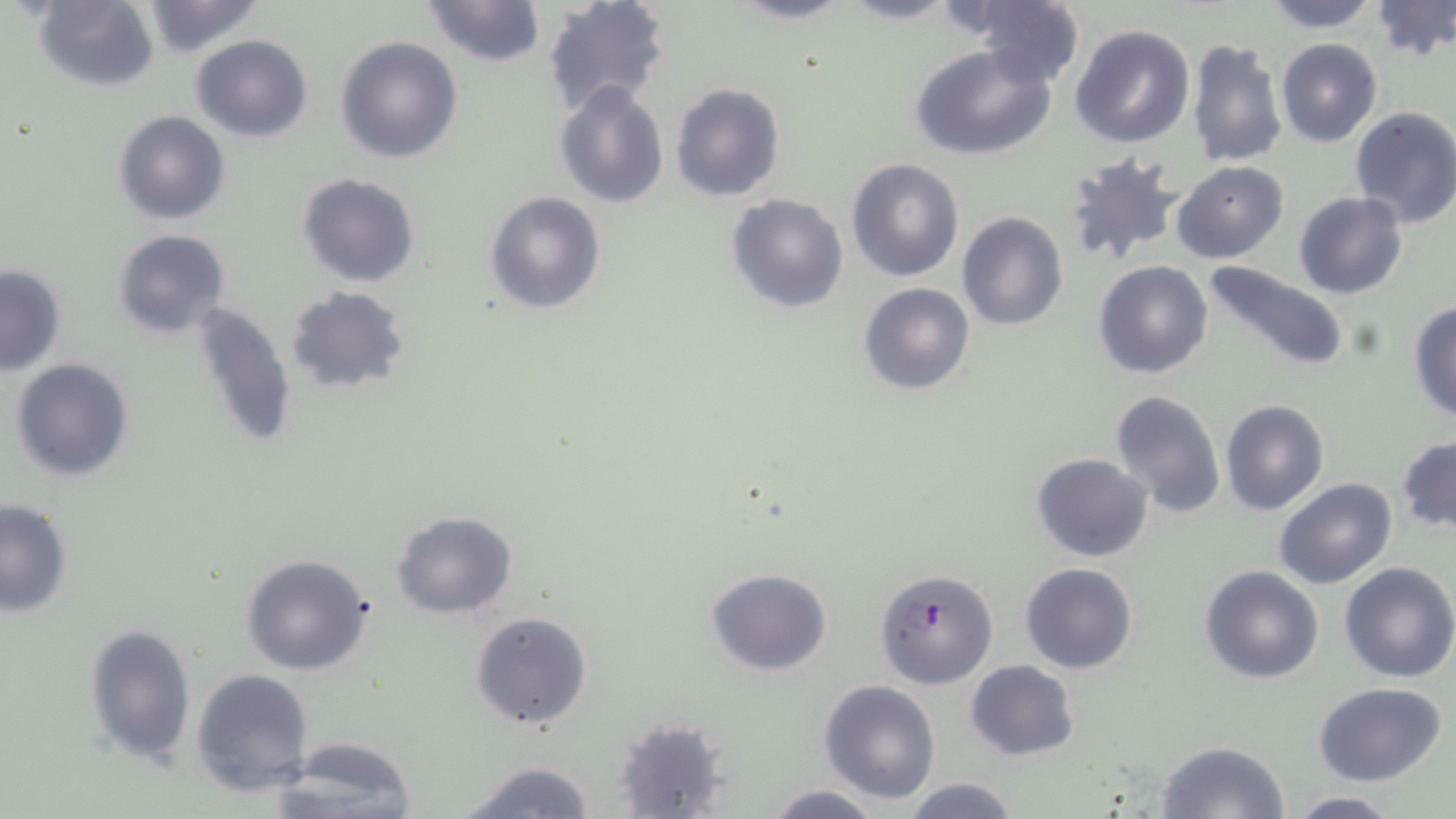

Approximate bounding boxes as named x1/y1/x2/y2 corners in pixels. Uninfected red blood cell locations: (x1=32, y1=0, x2=158, y2=91), (x1=137, y1=0, x2=268, y2=57), (x1=420, y1=0, x2=547, y2=69), (x1=541, y1=0, x2=672, y2=117), (x1=725, y1=0, x2=859, y2=25), (x1=834, y1=0, x2=963, y2=25), (x1=1259, y1=0, x2=1382, y2=32), (x1=1370, y1=0, x2=1456, y2=64), (x1=963, y1=4, x2=1086, y2=88), (x1=1070, y1=23, x2=1196, y2=150), (x1=190, y1=34, x2=313, y2=142), (x1=334, y1=35, x2=464, y2=164), (x1=1186, y1=37, x2=1288, y2=169), (x1=1275, y1=38, x2=1384, y2=147), (x1=909, y1=42, x2=1057, y2=161), (x1=553, y1=81, x2=669, y2=208), (x1=670, y1=82, x2=785, y2=202), (x1=1350, y1=105, x2=1456, y2=230), (x1=113, y1=110, x2=231, y2=225), (x1=1061, y1=148, x2=1185, y2=269), (x1=845, y1=156, x2=964, y2=282), (x1=1172, y1=162, x2=1290, y2=264), (x1=297, y1=174, x2=421, y2=288), (x1=484, y1=190, x2=606, y2=315), (x1=1293, y1=191, x2=1408, y2=299), (x1=725, y1=192, x2=850, y2=314), (x1=957, y1=211, x2=1068, y2=331), (x1=114, y1=229, x2=231, y2=339), (x1=1201, y1=258, x2=1349, y2=376), (x1=1094, y1=261, x2=1214, y2=380), (x1=1, y1=265, x2=67, y2=375), (x1=856, y1=282, x2=975, y2=395), (x1=284, y1=285, x2=410, y2=395), (x1=186, y1=300, x2=298, y2=453), (x1=1407, y1=300, x2=1456, y2=423), (x1=10, y1=357, x2=134, y2=482), (x1=1111, y1=389, x2=1227, y2=520), (x1=1221, y1=398, x2=1328, y2=516), (x1=1397, y1=436, x2=1456, y2=533), (x1=1030, y1=453, x2=1153, y2=562), (x1=1274, y1=478, x2=1397, y2=588), (x1=0, y1=500, x2=73, y2=618), (x1=391, y1=509, x2=518, y2=619), (x1=1312, y1=514, x2=1445, y2=657), (x1=240, y1=553, x2=374, y2=676), (x1=1019, y1=562, x2=1140, y2=675), (x1=1338, y1=562, x2=1456, y2=683), (x1=1199, y1=565, x2=1324, y2=684), (x1=706, y1=568, x2=833, y2=676), (x1=470, y1=611, x2=593, y2=730), (x1=82, y1=621, x2=196, y2=766), (x1=965, y1=659, x2=1081, y2=761), (x1=191, y1=667, x2=314, y2=798), (x1=819, y1=680, x2=942, y2=804), (x1=1312, y1=682, x2=1448, y2=786), (x1=610, y1=714, x2=733, y2=818), (x1=269, y1=736, x2=419, y2=817), (x1=1154, y1=741, x2=1290, y2=819), (x1=453, y1=757, x2=599, y2=818), (x1=899, y1=777, x2=1023, y2=819), (x1=763, y1=784, x2=883, y2=818), (x1=1286, y1=793, x2=1403, y2=819). Plasmodium falciparum-infected red blood cell locations: (x1=875, y1=568, x2=999, y2=689). Slide-level diagnosis: Plasmodium falciparum. Thin blood smear. Image is 1456×819 pixels. Single field of view. 1000x magnification. Light microscopy. May-Grünwald-Giemsa stain.